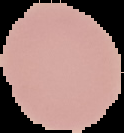
image type = segmented cell region with the area outside set to black
malaria status = uninfected
preparation = thin blood smear
image size = 124×133 pixels